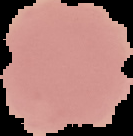
image size = 133×136 pixels
preparation = thin blood smear
result = no Plasmodium parasites seen
image type = segmented cell region on a black background